Classify this cell by malaria status.
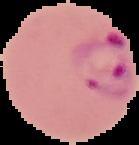

It is parasitized.

Summary:
  - Image size: 139×145 pixels
  - Image type: segmented cell region with the area outside set to black
  - Preparation: thin blood smear